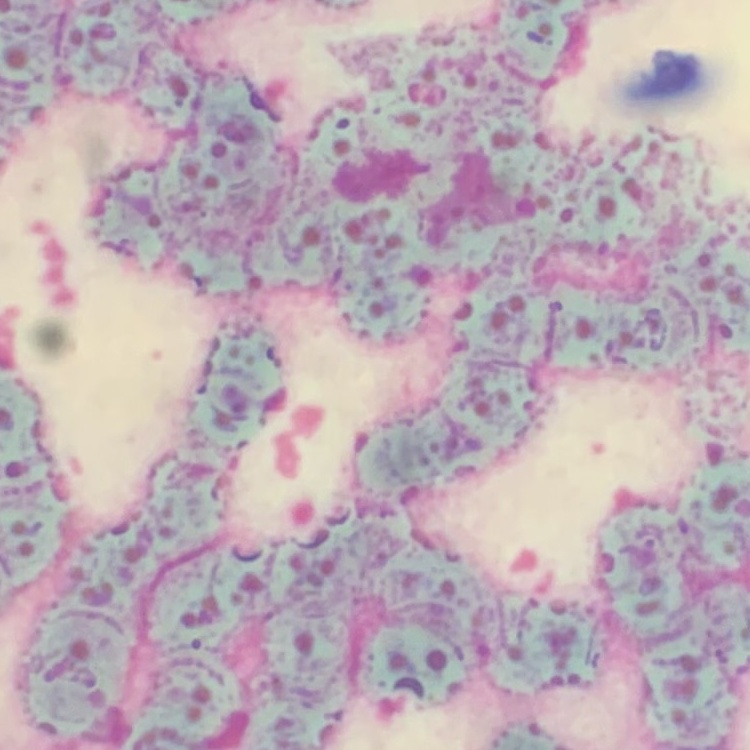

{
  "erythrocyte_morphology": "rouleaux formation",
  "preparation": "thin blood film",
  "stain": "Field's or Giemsa",
  "image_type": "one tile cut from a larger photomicrograph"
}